Evaluate for malaria.
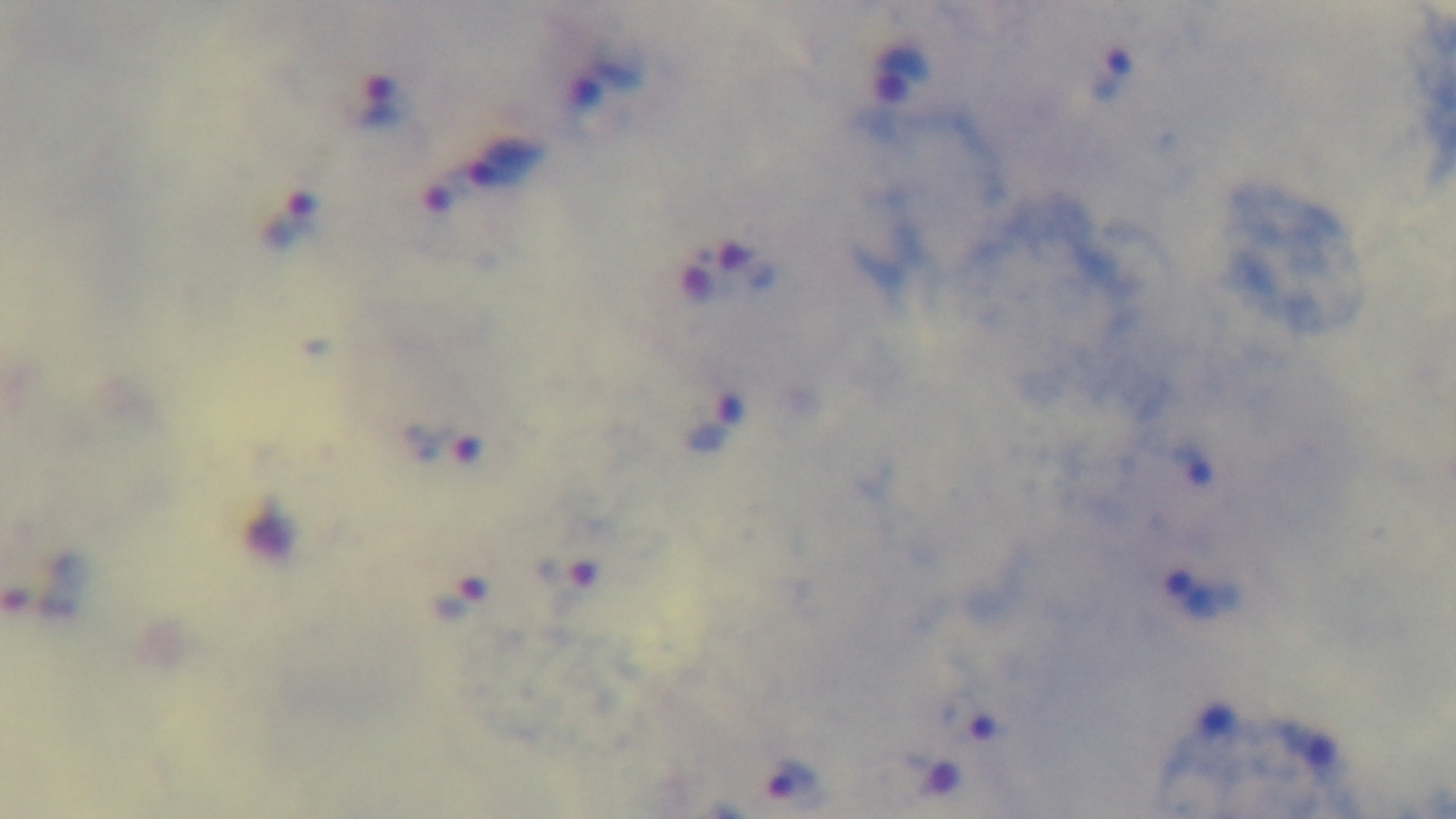

Infected.

stain = Giemsa
capture = mounted 4K digital camera
objective = 100x oil immersion
field of view = single
preparation = thick blood film
modality = light microscopy